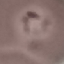
Summary:
  - Malaria status: parasitized
  - Preparation: thin blood smear
  - Image type: automatically extracted cell patch, resized to 64 × 64 pixels
  - Stain: Giemsa
  - Capture: smartphone through the microscope eyepiece